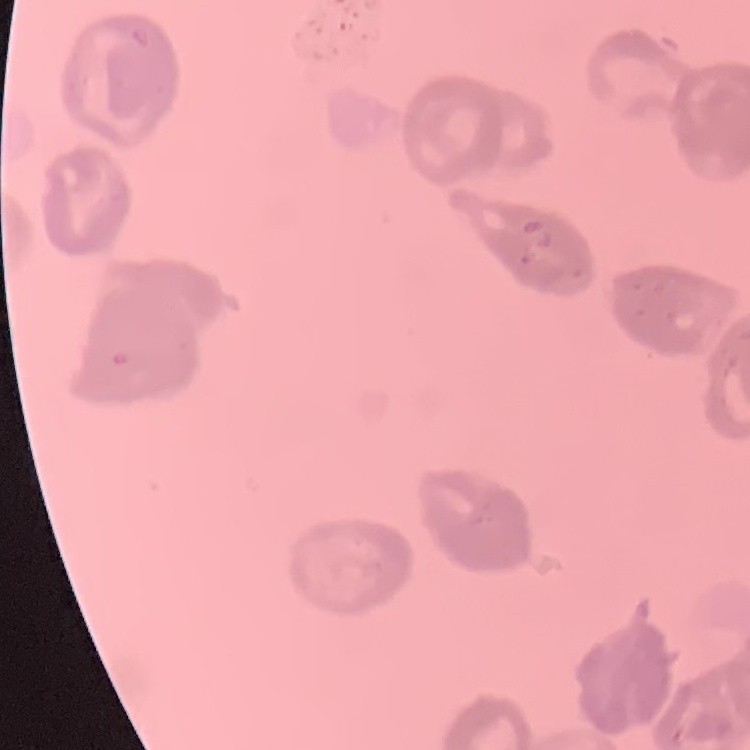
Summary:
  - Erythrocyte morphology: rouleaux formation
  - Stain: Field's or Giemsa
  - Image type: one tile cut from a larger photomicrograph
  - Preparation: thin blood film